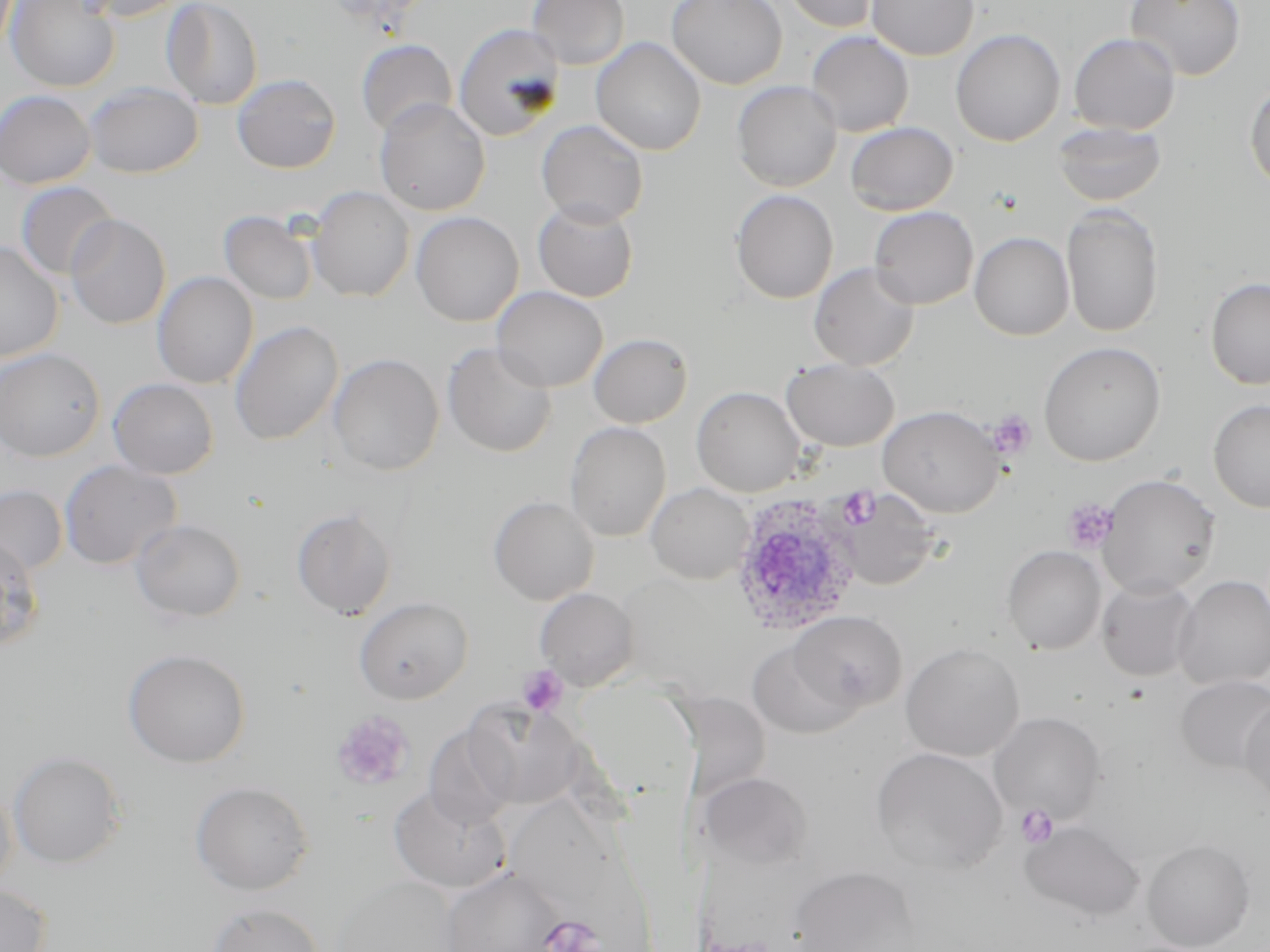 Approximate bounding boxes as [x1, y1, x2, y2] in pixels. Uninfected red blood cell locations: [6, 0, 121, 93], [73, 0, 190, 22], [161, 0, 263, 109], [527, 0, 630, 70], [666, 0, 787, 89], [781, 0, 882, 33], [867, 0, 979, 60], [1125, 0, 1246, 81], [453, 22, 565, 142], [950, 29, 1065, 146], [805, 31, 914, 137], [1069, 33, 1180, 135], [591, 37, 707, 156], [356, 40, 457, 136], [232, 74, 341, 174], [732, 80, 842, 192], [1245, 80, 1270, 192], [83, 82, 203, 178], [0, 89, 96, 189], [374, 98, 490, 216], [536, 120, 648, 227], [1052, 120, 1166, 207], [845, 122, 958, 216], [15, 181, 118, 281], [308, 186, 415, 302], [731, 189, 838, 304], [533, 199, 638, 302], [1061, 205, 1164, 338], [869, 206, 978, 309], [219, 210, 318, 305], [411, 211, 523, 327], [66, 214, 171, 329], [969, 232, 1074, 340], [0, 241, 64, 362], [809, 262, 920, 371], [152, 272, 258, 389], [1205, 277, 1270, 389], [492, 286, 608, 393], [230, 320, 344, 445], [588, 333, 693, 428], [442, 341, 557, 458], [1039, 341, 1166, 466], [0, 348, 105, 461], [328, 353, 444, 476], [782, 358, 900, 451], [108, 378, 218, 479], [691, 386, 805, 497], [1208, 400, 1270, 513], [878, 405, 1004, 517], [565, 421, 671, 542], [60, 460, 182, 570], [1097, 474, 1220, 597], [645, 482, 754, 584], [0, 485, 68, 576], [837, 490, 940, 590], [488, 495, 599, 605], [291, 506, 397, 619], [131, 518, 247, 623], [0, 536, 44, 650], [1002, 545, 1106, 655], [1173, 575, 1270, 689], [1097, 577, 1200, 681], [534, 587, 638, 690], [355, 597, 473, 703], [787, 610, 906, 715], [747, 639, 859, 738], [901, 642, 1025, 761], [123, 648, 251, 767], [1176, 676, 1270, 775], [1239, 694, 1270, 808], [463, 700, 585, 810], [989, 711, 1105, 824], [423, 725, 516, 830], [871, 747, 1007, 875], [7, 750, 126, 869], [700, 771, 813, 870], [0, 780, 18, 896], [191, 781, 314, 895], [389, 786, 510, 893], [1020, 820, 1145, 921], [1142, 839, 1255, 951], [441, 866, 567, 952], [789, 867, 920, 951], [332, 875, 460, 952], [0, 883, 52, 952], [206, 902, 325, 952]. Plasmodium ovale-infected red blood cell locations: [730, 493, 867, 635]. Platelet locations: [987, 409, 1036, 459], [1062, 498, 1120, 554], [517, 665, 568, 716], [331, 710, 414, 791], [1015, 805, 1057, 849]. Slide-level diagnosis: Plasmodium ovale. Thin blood film. Image is 1270×952 pixels. Single field of view. May-Grünwald-Giemsa-stained preparation. Optical microscopy. 1000x magnification.